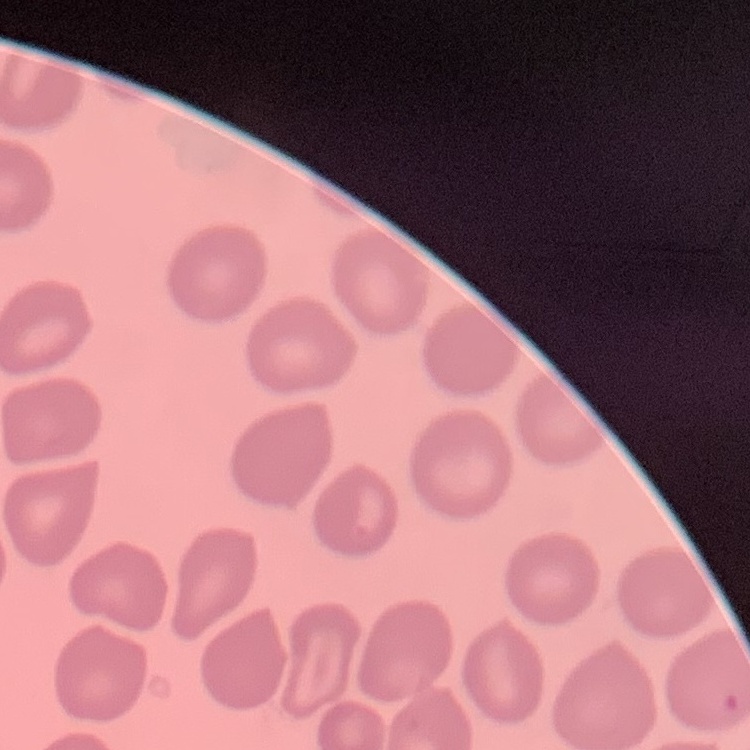
Summary:
  - Red blood cell morphology: no rouleaux formation
  - Stain: Field's or Giemsa
  - Image type: one tile cut from a larger photomicrograph
  - Preparation: thin blood film